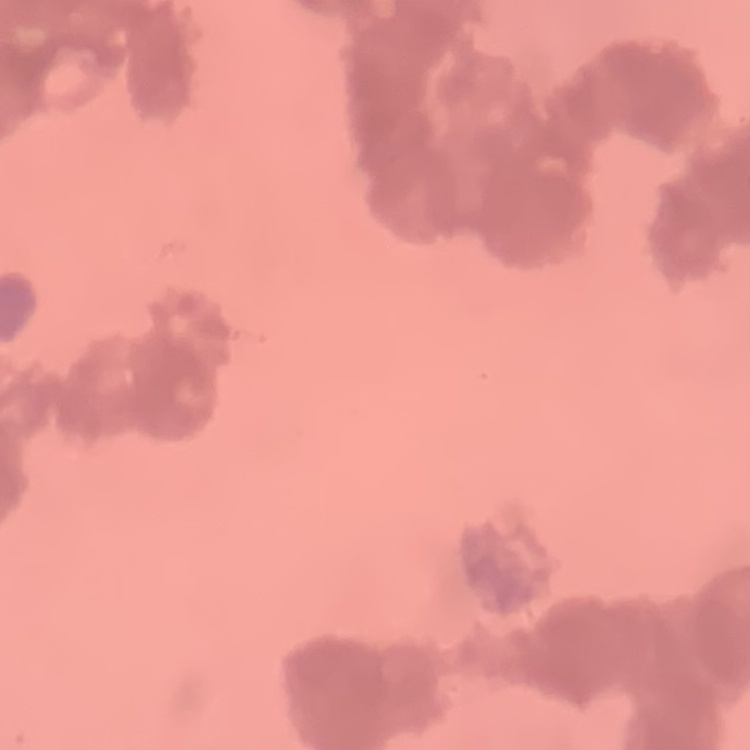
The red blood cells exhibit rouleaux formation. Field's or Giemsa stain. Thin peripheral smear. Square crop of a larger photomicrograph.